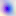

400x magnification. Photomicrograph. Toxoplasma gondii is seen.